Outline each blood parasite and name the species.
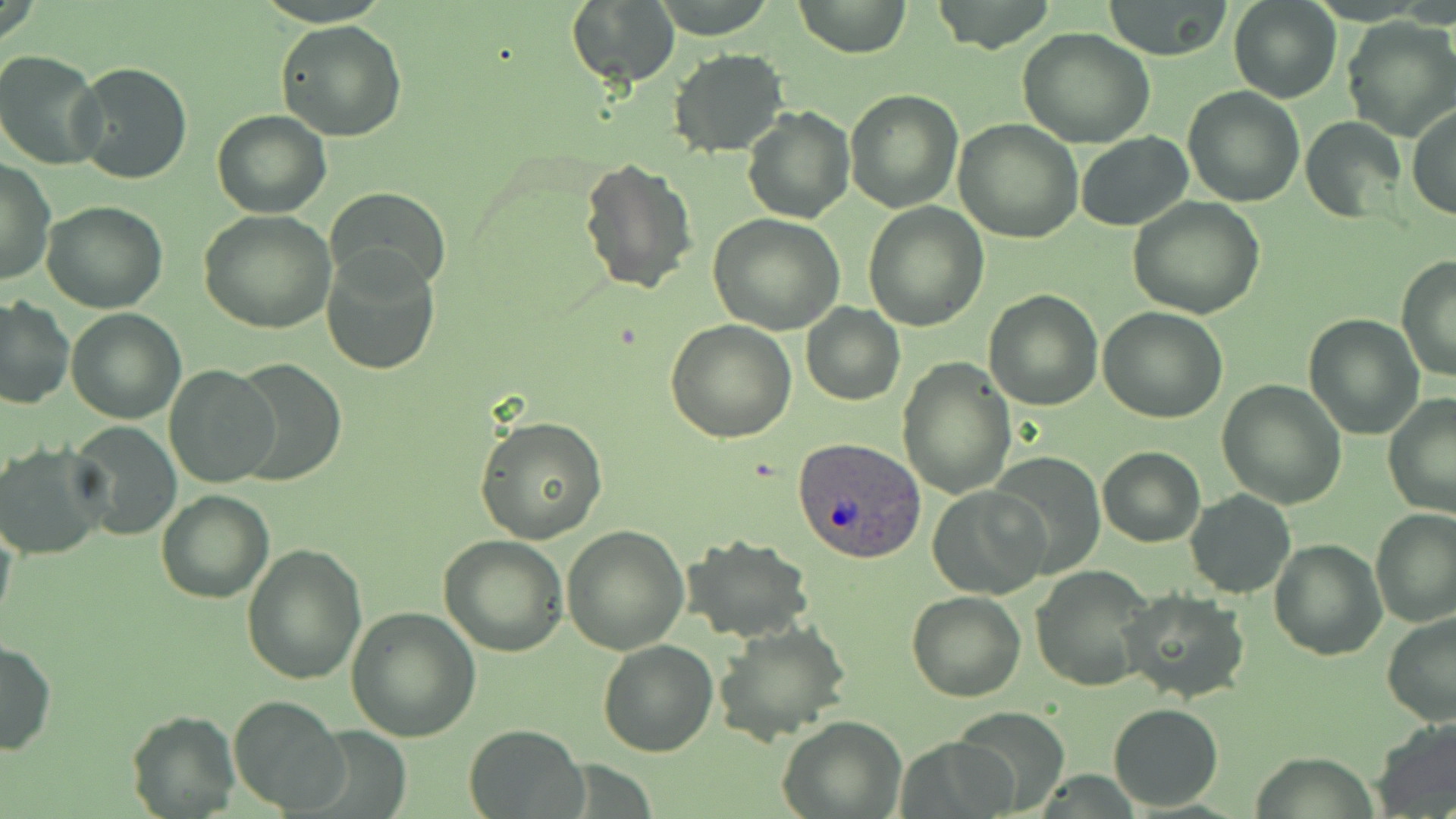

Approximate bounding boxes as (x1,y1)-(x2,y2) corner pairs in pixels.
Plasmodium ovale-infected red blood cells: (793,435)-(927,562).
No Plasmodium falciparum, Plasmodium malariae, Plasmodium vivax, Babesia divergens, or Trypanosoma brucei observed.

Summary:
  - Uninfected red blood cell locations: (567,0)-(681,91), (793,0)-(911,58), (929,0)-(1059,54), (1102,0)-(1235,61), (1228,0)-(1341,102), (275,18)-(407,142), (1342,18)-(1456,141), (1018,28)-(1155,149), (0,49)-(108,169), (670,49)-(788,158), (74,62)-(192,185), (1183,86)-(1304,206), (843,87)-(963,212), (741,105)-(854,224), (1407,105)-(1456,222), (212,110)-(332,218), (1302,117)-(1405,223), (953,120)-(1083,243), (1077,133)-(1193,228), (578,157)-(698,296), (1,158)-(55,286), (328,186)-(450,299), (1127,196)-(1266,319), (40,202)-(167,314), (864,202)-(988,332), (197,209)-(336,334), (707,215)-(844,334), (321,246)-(443,375), (1395,255)-(1456,382), (983,289)-(1103,410), (1,295)-(74,410), (802,304)-(905,406), (65,309)-(186,424), (1098,309)-(1227,424), (1303,313)-(1425,440), (666,321)-(796,442), (898,357)-(1015,498), (229,360)-(347,486), (166,363)-(280,486), (1216,378)-(1348,509), (1382,394)-(1456,520), (473,413)-(607,545), (67,422)-(181,540), (3,444)-(112,562), (1098,446)-(1205,546), (988,454)-(1105,576), (929,485)-(1049,597), (1185,489)-(1296,598), (156,490)-(273,604), (1370,507)-(1456,628), (0,512)-(18,637), (562,524)-(690,654), (682,535)-(814,643), (439,536)-(568,658), (1269,538)-(1387,659), (240,543)-(368,685), (1032,565)-(1156,693), (1122,588)-(1249,703), (906,591)-(1025,703), (346,605)-(481,741), (1380,611)-(1456,727), (713,621)-(850,745), (0,638)-(57,757), (597,639)-(718,757), (228,694)-(349,816), (1107,703)-(1223,812), (947,708)-(1069,816), (127,710)-(239,819), (778,715)-(907,819), (1373,715)-(1456,816), (463,725)-(587,817), (900,736)-(1016,819)
  - Slide-level diagnosis: Plasmodium ovale
  - Stain: May-Grünwald-Giemsa
  - Modality: optical microscopy
  - Field of view: single
  - Preparation: thin blood film
  - Image size: 1456×819 pixels
  - Magnification: 1000x